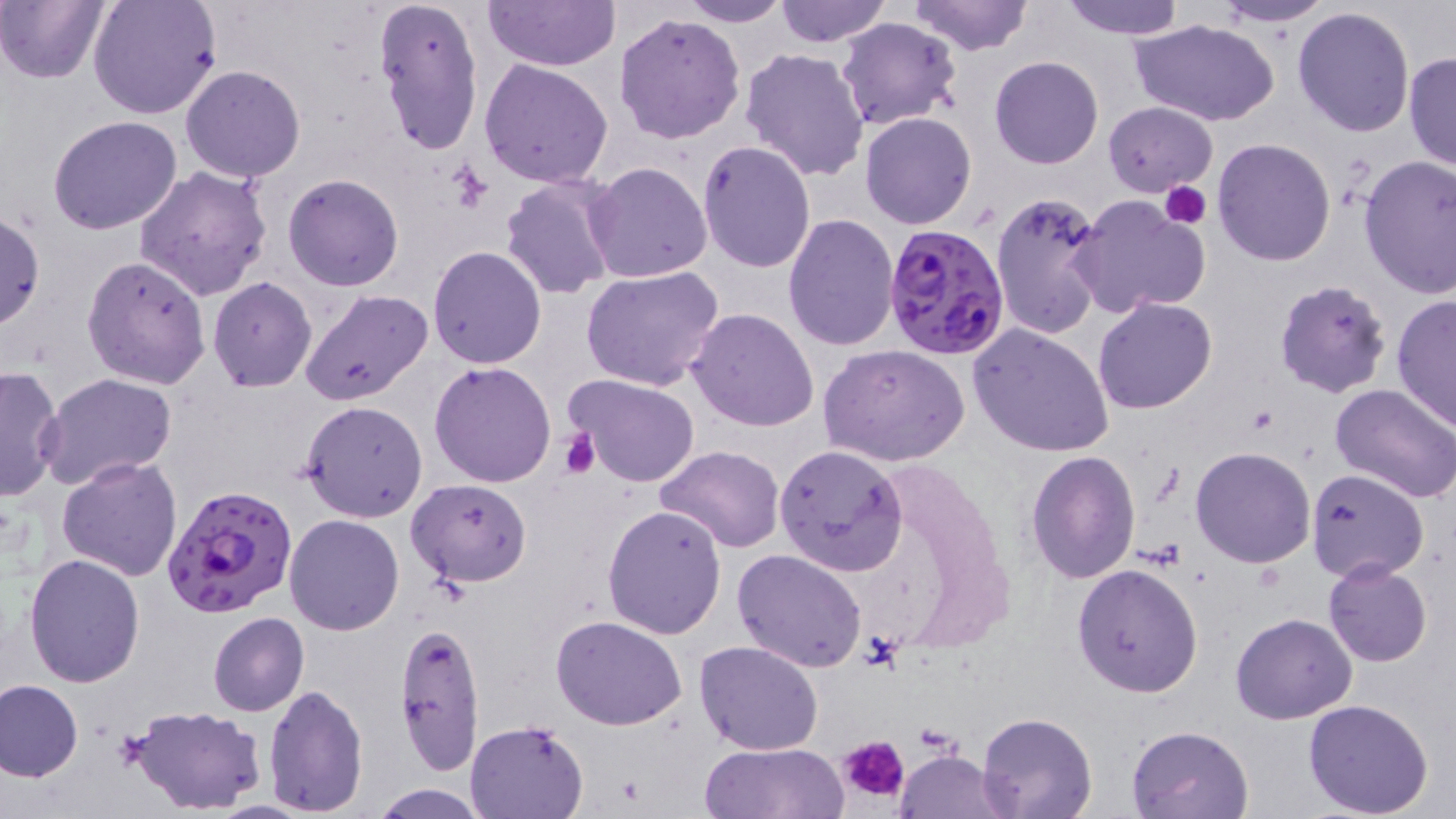

Summary:
  - Coordinate format: approximate bounding boxes as [x1, y1, x2, y2] in pixels
  - Uninfected red blood cell locations: [86, 0, 220, 120], [371, 0, 483, 156], [483, 0, 621, 72], [676, 0, 794, 26], [774, 0, 891, 47], [908, 0, 1034, 56], [1060, 0, 1187, 38], [0, 1, 108, 84], [1206, 1, 1337, 27], [1293, 6, 1416, 139], [614, 12, 745, 143], [836, 17, 963, 132], [1131, 19, 1279, 127], [739, 46, 871, 182], [1404, 49, 1456, 174], [989, 56, 1104, 169], [480, 59, 614, 188], [182, 65, 306, 183], [1102, 101, 1218, 198], [860, 112, 976, 229], [48, 116, 182, 236], [1211, 137, 1336, 266], [699, 140, 817, 271], [1358, 155, 1456, 298], [583, 161, 712, 283], [135, 165, 272, 301], [282, 173, 405, 291], [500, 174, 620, 301], [991, 188, 1110, 342], [1070, 194, 1211, 319], [0, 210, 44, 331], [782, 213, 900, 352], [428, 245, 546, 367], [82, 254, 212, 390], [581, 266, 725, 392], [207, 277, 317, 392], [1275, 279, 1391, 399], [299, 288, 434, 406], [1391, 291, 1456, 433], [1093, 297, 1218, 414], [688, 308, 819, 431], [968, 323, 1115, 457], [817, 344, 970, 466], [430, 360, 557, 487], [0, 364, 64, 502], [37, 374, 180, 493], [568, 375, 699, 488], [1329, 380, 1456, 503], [300, 400, 428, 522], [656, 445, 785, 552], [777, 445, 906, 577], [1189, 446, 1317, 569], [1026, 450, 1141, 583], [55, 456, 183, 581], [1307, 469, 1430, 583], [407, 478, 531, 586], [602, 504, 727, 639], [284, 514, 405, 636], [733, 550, 867, 672], [24, 553, 146, 688], [1323, 561, 1433, 667], [1071, 563, 1203, 699], [208, 611, 309, 716], [1231, 611, 1357, 723], [551, 615, 689, 731], [395, 618, 488, 775], [695, 639, 822, 753], [0, 679, 85, 783], [262, 684, 368, 817], [1302, 699, 1434, 818], [131, 705, 266, 816], [976, 712, 1096, 819], [465, 720, 589, 818], [1128, 724, 1255, 818], [698, 741, 846, 819], [894, 749, 1011, 819], [370, 783, 489, 818]
  - Platelet locations: [1160, 181, 1212, 230], [557, 429, 600, 479], [840, 735, 909, 804]
  - Plasmodium falciparum-infected red blood cell locations: [881, 222, 1012, 360], [161, 483, 299, 620]
  - Slide-level diagnosis: Plasmodium falciparum
  - Stain: May-Grünwald-Giemsa
  - Image size: 1456×819 pixels
  - Magnification: 1000x
  - Preparation: thin blood smear
  - Field of view: one of a larger specimen
  - Modality: light microscopy